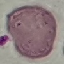 Result: negative for malaria parasites. Photographed with a smartphone camera at the microscope eyepiece. Thin blood film. Giemsa stain. Cell patch, automatically extracted from a larger field of view and resized to 64 × 64 pixels.